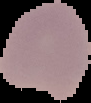
image size = 91×103 pixels
image type = cell region segmented out of the field of view; surrounding area masked to black
preparation = thin blood film
result = malaria parasites identified